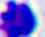 Captured at 400x magnification. Photomicrograph. A white blood cell is shown.